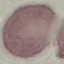

Summary:
  - Malaria status: uninfected
  - Image type: automatically extracted cell patch, resized to 64 × 64 pixels
  - Preparation: thin blood film
  - Stain: Giemsa
  - Capture: smartphone through the microscope eyepiece